Name the blood parasite species.
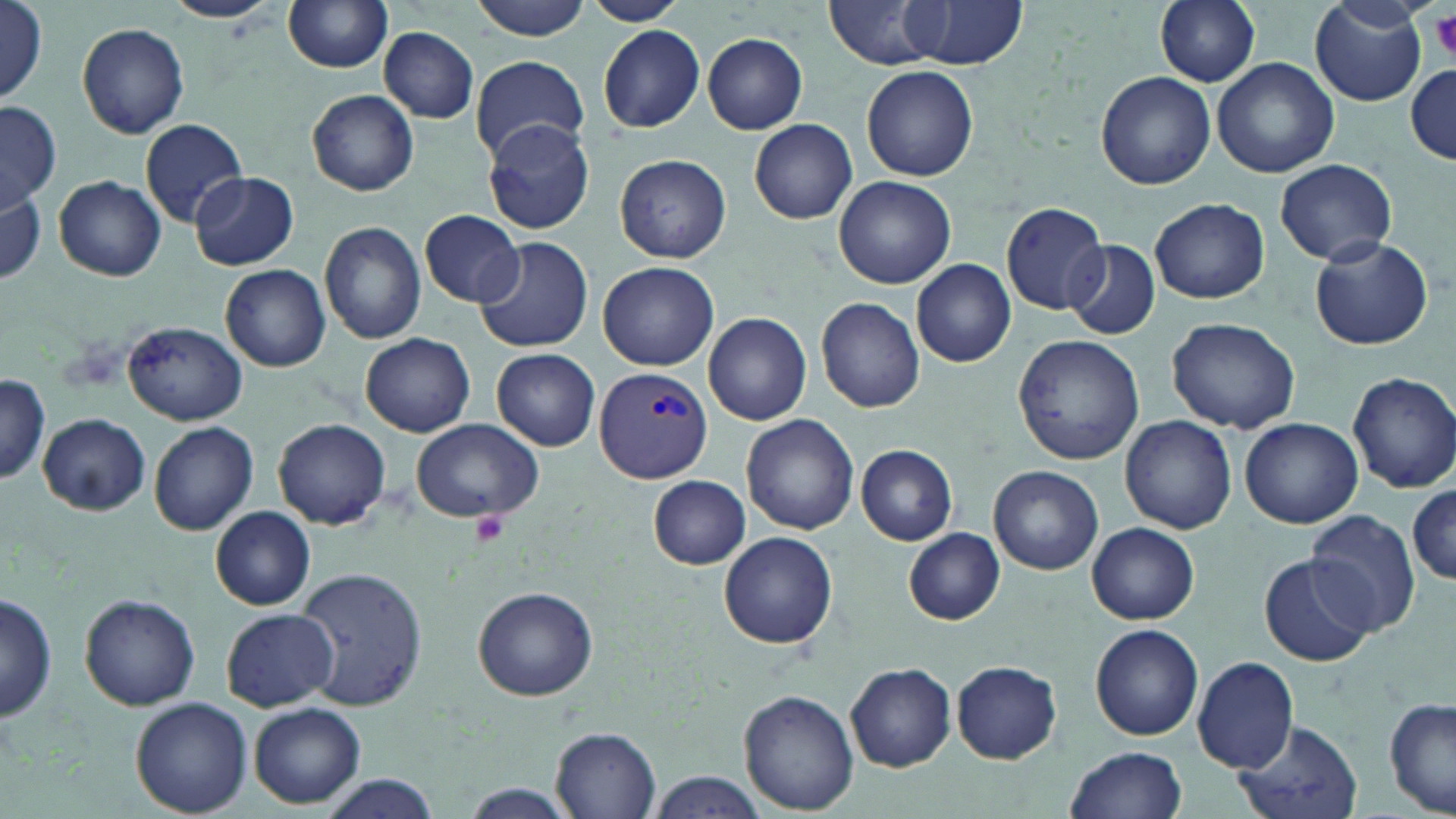

Plasmodium vivax.

Approximate bounding boxes as [x1, y1, x2, y2] in pixels. Platelet locations: [1430, 13, 1456, 60], [470, 509, 508, 545]. Plasmodium vivax-infected red blood cell locations: [593, 366, 713, 484]. Uninfected red blood cell locations: [163, 0, 282, 23], [282, 0, 395, 72], [467, 0, 593, 39], [583, 0, 685, 25], [826, 0, 944, 70], [1154, 0, 1261, 87], [1308, 0, 1428, 107], [898, 1, 1025, 69], [0, 2, 49, 105], [78, 23, 190, 139], [597, 25, 703, 132], [378, 27, 478, 121], [702, 33, 808, 134], [471, 54, 588, 162], [1212, 58, 1338, 179], [1407, 64, 1455, 161], [862, 66, 978, 182], [1096, 71, 1216, 189], [308, 90, 418, 197], [0, 101, 60, 209], [139, 117, 249, 228], [750, 118, 857, 223], [482, 120, 594, 235], [615, 153, 731, 263], [1275, 158, 1397, 266], [189, 171, 299, 271], [52, 175, 167, 280], [835, 176, 956, 289], [0, 187, 45, 288], [1150, 198, 1269, 305], [1001, 202, 1108, 314], [419, 210, 525, 306], [318, 222, 427, 346], [1309, 236, 1434, 350], [473, 237, 592, 354], [1063, 239, 1159, 339], [912, 257, 1016, 367], [598, 260, 720, 371], [221, 264, 330, 372], [816, 297, 925, 413], [702, 312, 810, 425], [1166, 317, 1301, 433], [123, 321, 248, 425], [359, 332, 475, 436], [1013, 334, 1145, 465], [492, 348, 600, 452], [1347, 371, 1456, 494], [0, 375, 50, 485], [39, 414, 149, 513], [741, 414, 859, 535], [1121, 415, 1237, 535], [411, 417, 542, 523], [274, 418, 389, 530], [1240, 418, 1362, 528], [149, 420, 259, 536], [855, 444, 958, 545], [989, 465, 1103, 575], [648, 476, 752, 569], [1409, 479, 1456, 590], [210, 506, 316, 611], [1306, 509, 1422, 636], [1087, 522, 1200, 624], [903, 527, 1005, 625], [719, 532, 838, 648], [1259, 555, 1375, 667], [295, 566, 428, 710], [472, 584, 599, 700], [1, 593, 58, 721], [79, 593, 199, 710], [221, 609, 337, 712], [1090, 624, 1203, 741], [1191, 654, 1299, 775], [845, 660, 956, 772], [952, 661, 1061, 762], [738, 688, 858, 813], [1385, 697, 1455, 819], [130, 698, 252, 818], [249, 703, 367, 808], [1231, 717, 1365, 819], [552, 727, 662, 817], [1067, 745, 1189, 819], [648, 772, 768, 818], [316, 773, 442, 819], [456, 785, 583, 817]. Optical microscopy. One field of a larger specimen. 1000x magnification. Image is 1456×819 pixels. Thin blood film. May-Grünwald-Giemsa stain.